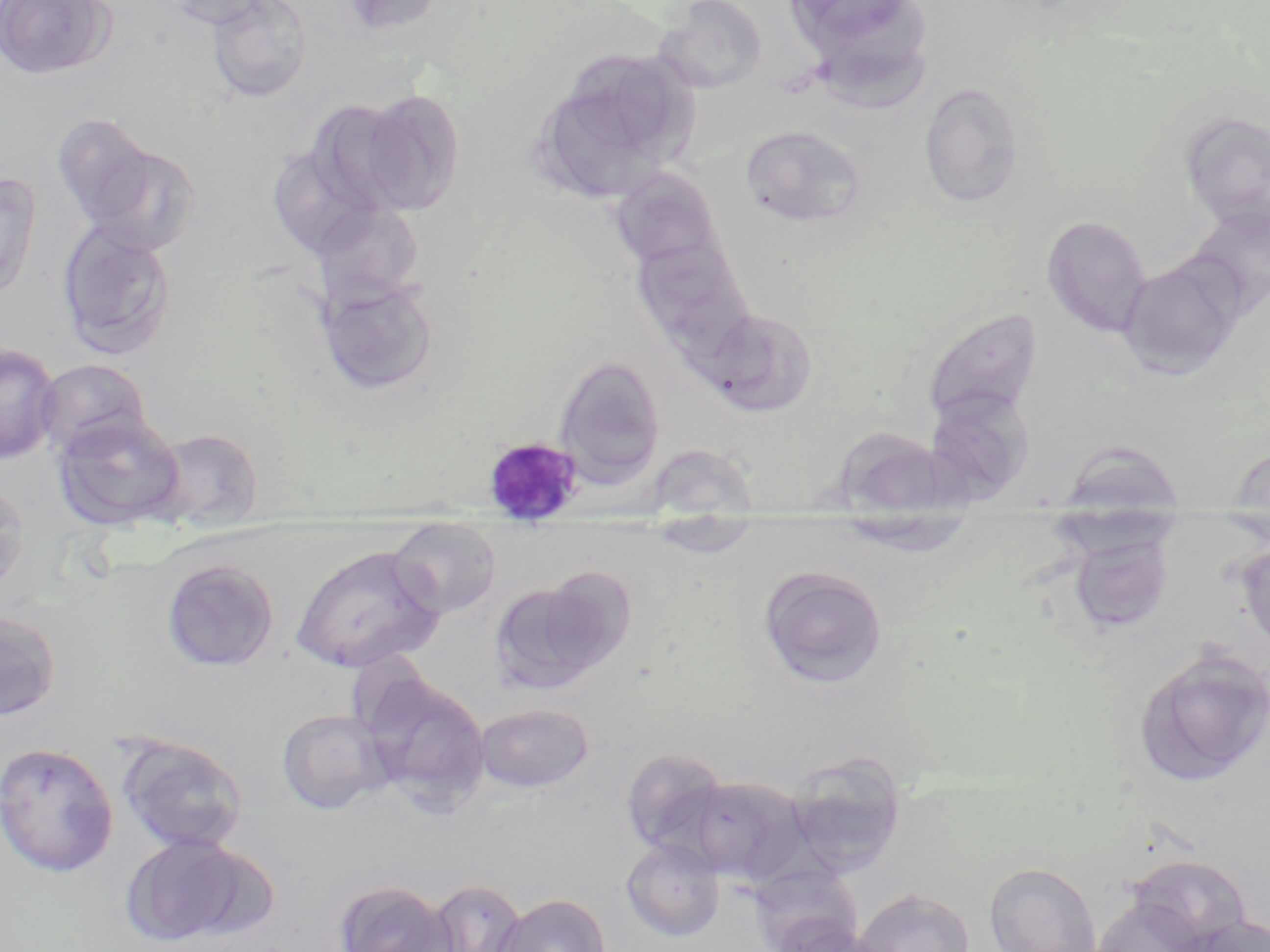

Summary:
  - Coordinate format: approximate bounding boxes as named x1/y1/x2/y2 corners in pixels
  - Plasmodium malariae-infected red blood cell locations: (x1=482, y1=435, x2=585, y2=521)
  - Uninfected red blood cell locations: (x1=0, y1=0, x2=115, y2=80), (x1=160, y1=0, x2=277, y2=29), (x1=337, y1=0, x2=449, y2=37), (x1=781, y1=0, x2=929, y2=69), (x1=204, y1=1, x2=313, y2=103), (x1=655, y1=1, x2=769, y2=93), (x1=529, y1=48, x2=699, y2=205), (x1=917, y1=81, x2=1027, y2=209), (x1=356, y1=88, x2=465, y2=215), (x1=1180, y1=109, x2=1270, y2=231), (x1=50, y1=113, x2=158, y2=230), (x1=739, y1=124, x2=869, y2=229), (x1=81, y1=140, x2=204, y2=257), (x1=265, y1=145, x2=382, y2=260), (x1=608, y1=168, x2=725, y2=275), (x1=0, y1=169, x2=42, y2=301), (x1=310, y1=201, x2=425, y2=305), (x1=1185, y1=203, x2=1270, y2=318), (x1=1041, y1=215, x2=1153, y2=338), (x1=56, y1=219, x2=178, y2=361), (x1=631, y1=234, x2=756, y2=354), (x1=1117, y1=255, x2=1245, y2=380), (x1=317, y1=277, x2=439, y2=396), (x1=700, y1=307, x2=819, y2=416), (x1=921, y1=308, x2=1045, y2=427), (x1=0, y1=342, x2=62, y2=465), (x1=552, y1=355, x2=666, y2=485), (x1=35, y1=359, x2=153, y2=457), (x1=922, y1=386, x2=1036, y2=504), (x1=52, y1=412, x2=186, y2=532), (x1=832, y1=427, x2=960, y2=517), (x1=149, y1=428, x2=265, y2=529), (x1=1054, y1=439, x2=1187, y2=513), (x1=645, y1=443, x2=759, y2=514), (x1=1225, y1=444, x2=1270, y2=514), (x1=0, y1=475, x2=30, y2=600), (x1=831, y1=513, x2=978, y2=557), (x1=639, y1=517, x2=765, y2=559), (x1=388, y1=520, x2=502, y2=618), (x1=1064, y1=524, x2=1179, y2=638), (x1=1235, y1=539, x2=1270, y2=657), (x1=291, y1=544, x2=445, y2=673), (x1=160, y1=558, x2=280, y2=673), (x1=757, y1=565, x2=889, y2=690), (x1=490, y1=574, x2=632, y2=697), (x1=0, y1=610, x2=62, y2=722), (x1=1130, y1=646, x2=1269, y2=790), (x1=360, y1=672, x2=492, y2=812), (x1=474, y1=702, x2=594, y2=793), (x1=277, y1=708, x2=391, y2=814), (x1=116, y1=734, x2=250, y2=854), (x1=0, y1=742, x2=119, y2=877), (x1=620, y1=747, x2=730, y2=858), (x1=783, y1=751, x2=908, y2=880), (x1=680, y1=774, x2=810, y2=885), (x1=119, y1=834, x2=256, y2=947), (x1=620, y1=838, x2=725, y2=942), (x1=1124, y1=853, x2=1252, y2=949), (x1=983, y1=862, x2=1102, y2=952), (x1=752, y1=877, x2=865, y2=952), (x1=332, y1=880, x2=457, y2=952), (x1=424, y1=880, x2=530, y2=952), (x1=854, y1=887, x2=975, y2=952), (x1=493, y1=894, x2=611, y2=952), (x1=1088, y1=896, x2=1208, y2=952), (x1=1175, y1=915, x2=1270, y2=952), (x1=769, y1=916, x2=880, y2=952)
  - Slide-level diagnosis: Plasmodium malariae
  - Image size: 1270×952 pixels
  - Field of view: one of a larger specimen
  - Preparation: thin blood film
  - Stain: May-Grünwald-Giemsa
  - Magnification: 1000x
  - Modality: light microscopy